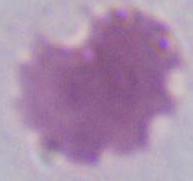 Photomicrograph. A red blood cell is shown. Captured at 1000x magnification.